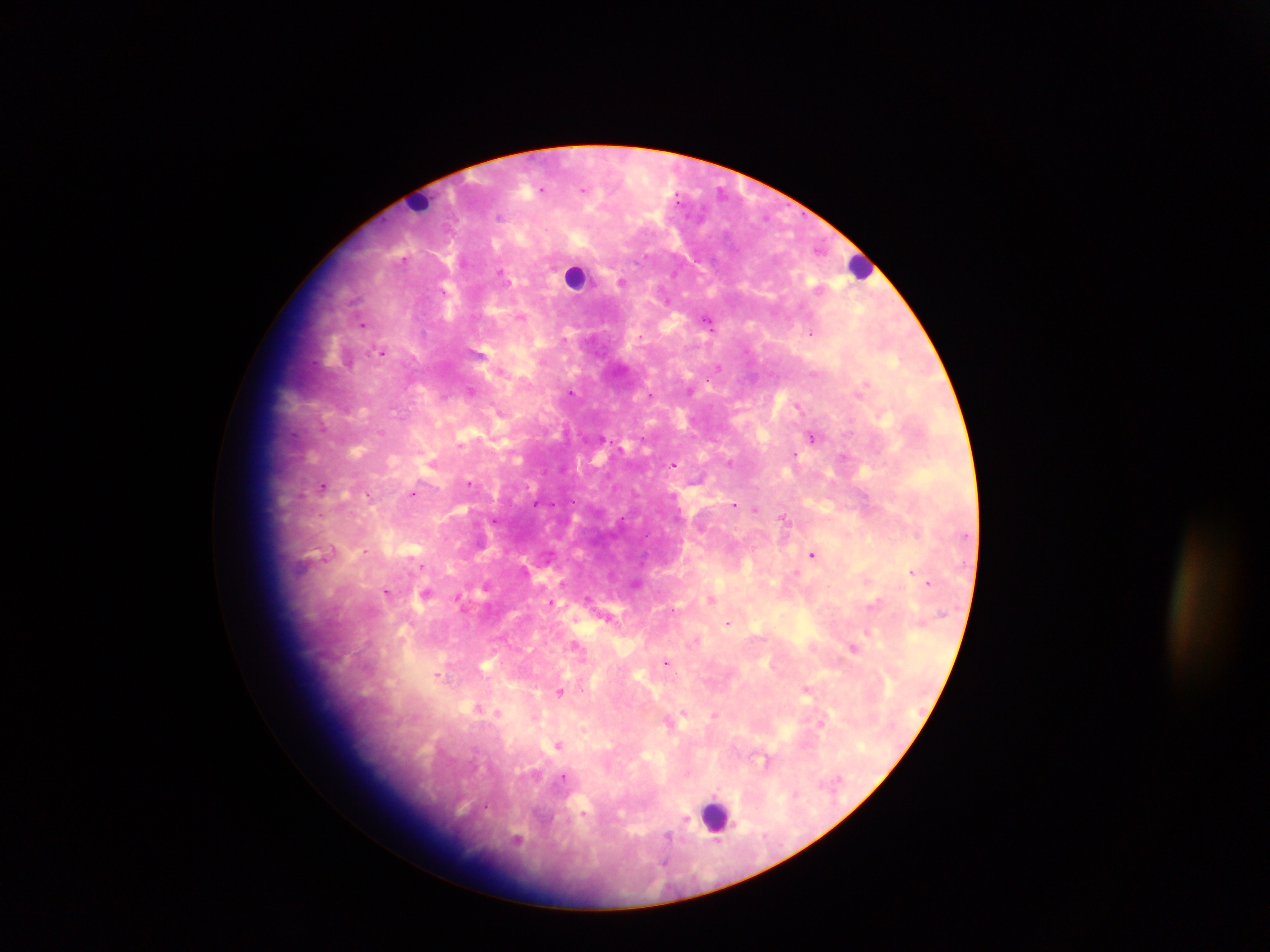
Approximate centers as x y in pixels.
Summary:
  - Leukocyte locations: 419 201; 861 266; 576 277; 716 814
  - Malaria parasite locations: 541 189; 583 189; 500 216; 403 260; 501 272; 622 281; 521 317; 706 319; 362 324; 812 332; 565 339; 381 351; 719 367; 501 371; 814 373; 470 391; 690 391; 572 392; 650 395; 798 406; 498 411; 323 428; 380 431; 812 437; 602 438; 460 445; 795 456; 843 456; 729 464; 673 465; 469 482; 324 486; 413 494; 300 495; 368 495; 673 496; 535 505; 734 505; 755 510; 784 518; 495 520; 365 550; 812 554; 327 555; 422 566; 911 572; 929 582; 636 583; 486 586; 387 592; 426 592; 458 598; 588 598; 712 599; 551 601; 608 617; 728 623; 868 632; 696 640; 576 646; 854 649; 667 662; 437 676; 806 689; 560 691; 479 707; 487 710; 497 712; 683 712; 715 715; 558 744; 563 777; 685 819; 668 837; 516 840; 717 842; 664 860
  - Country: Ghana
  - Preparation: thick blood smear
  - Capture: mobile-phone photograph through a microscope
  - Field of view: single
  - Image size: 1270×952 pixels